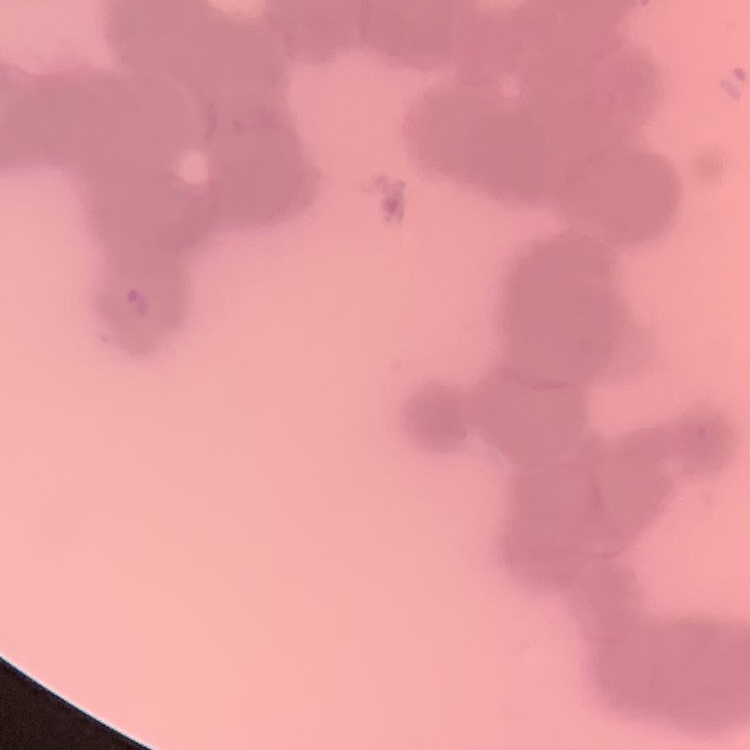
Summary:
  - Red blood cell morphology: rouleaux formation
  - Stain: Field's or Giemsa
  - Preparation: thin blood smear
  - Image type: square crop of a larger photomicrograph